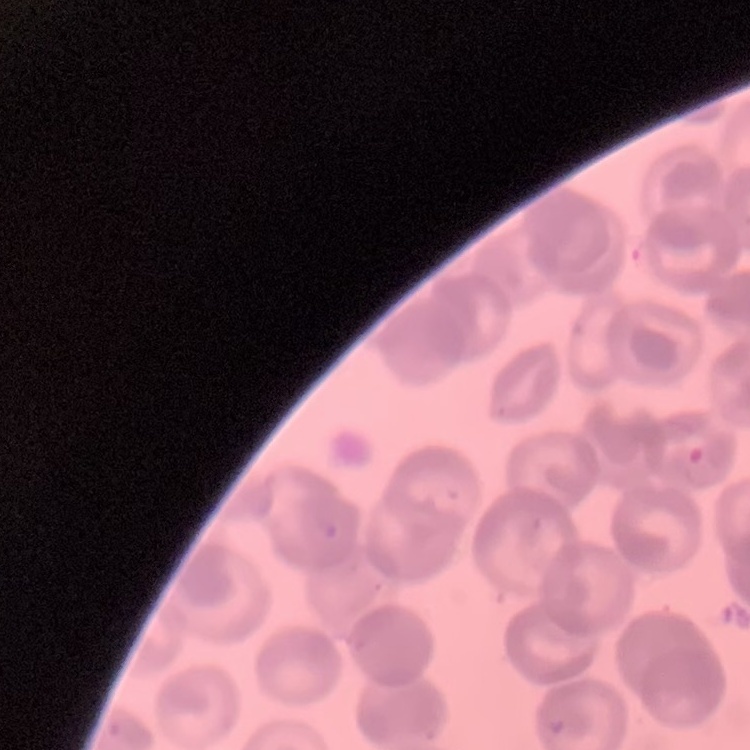

Summary:
  - Erythrocyte morphology: rouleaux formation
  - Image type: square crop of a larger photomicrograph
  - Stain: Field's or Giemsa
  - Preparation: thin blood film